Comment on the morphology of the red blood cells.
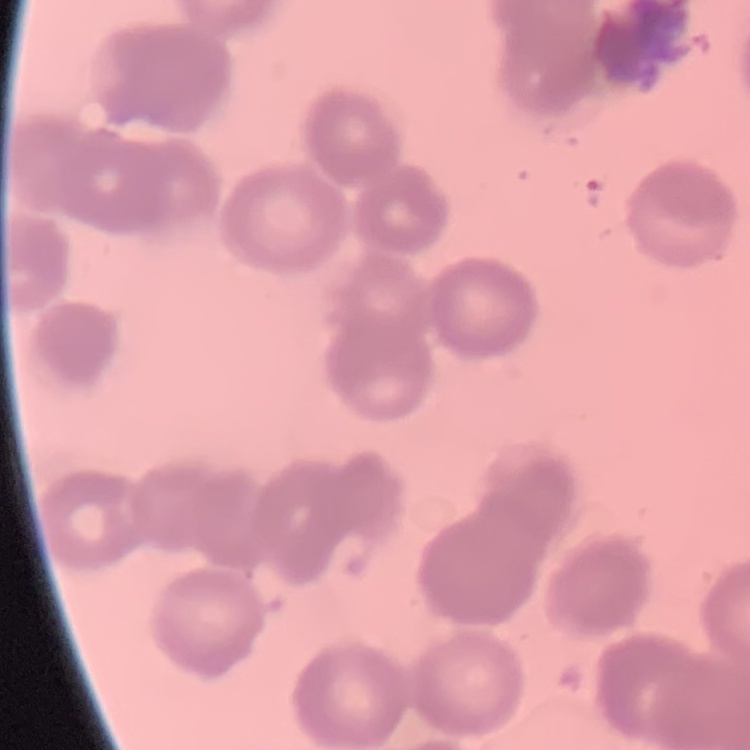

Rouleaux formation.

Field's or Giemsa stain. One tile cut from a larger photomicrograph. Thin blood film.